Name the cell type shown.
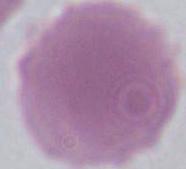
An erythrocyte.

1000x magnification. Micrograph.